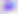 Toxoplasma gondii is seen. Micrograph. 400x magnification.